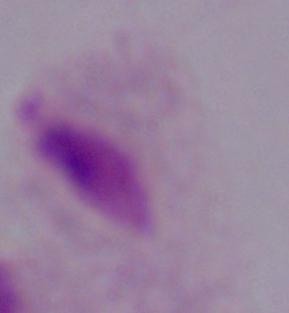 A trichomonad is seen. Micrograph. 1000x magnification.